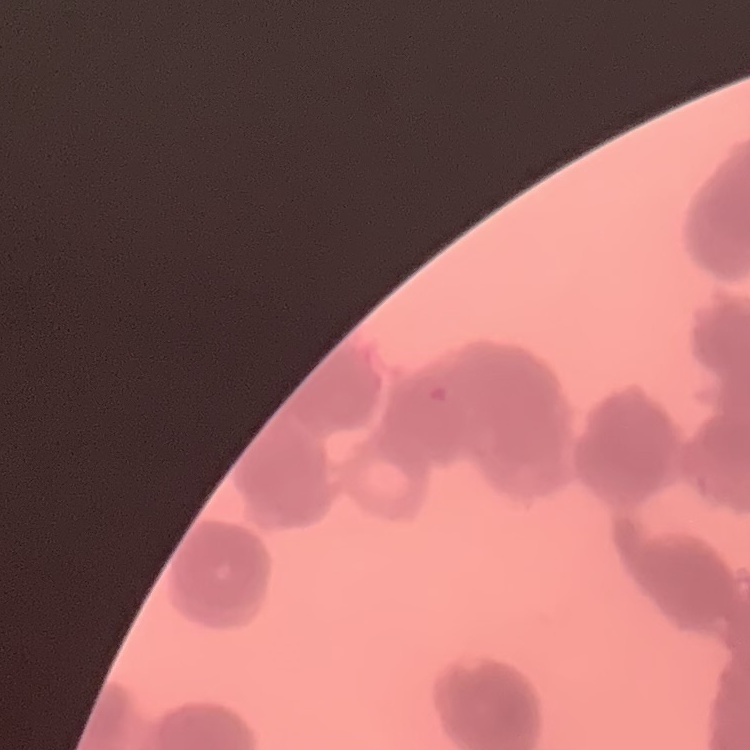

Summary:
  - Red blood cell morphology: rouleaux formation
  - Stain: Field's or Giemsa
  - Preparation: thin peripheral smear
  - Image type: square crop of a larger photomicrograph